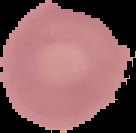

Cell region segmented out of the field of view; the surrounding area is masked to black. Result: no malaria parasites seen. From a thin blood smear. Image is 136×133 pixels.